Assess for malaria.
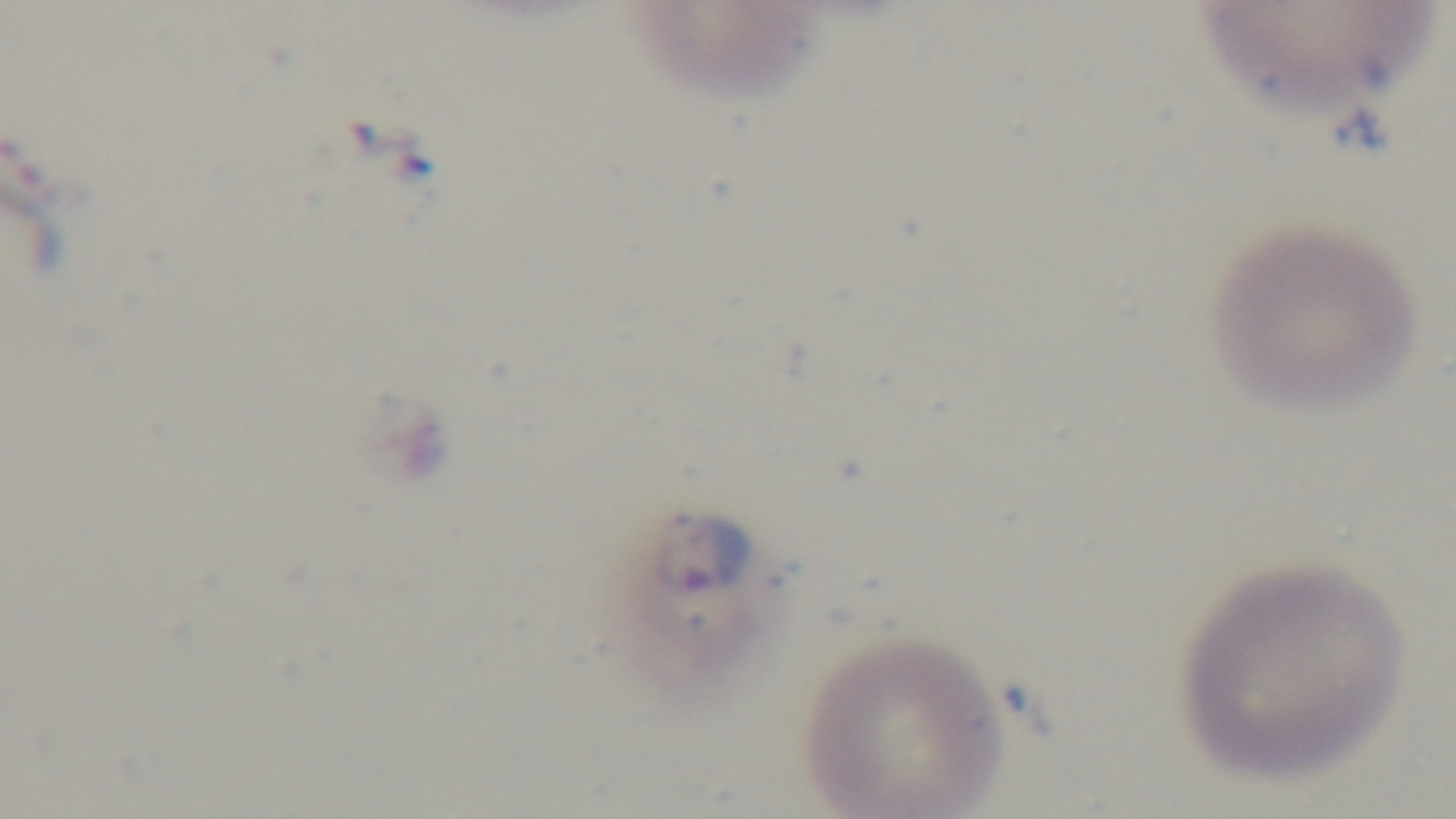
Infected.

modality = light microscopy
stain = Giemsa
objective = 100x oil immersion
field of view = single
capture = mounted 4K digital camera
preparation = thin blood film